Describe the morphology of the red blood cells.
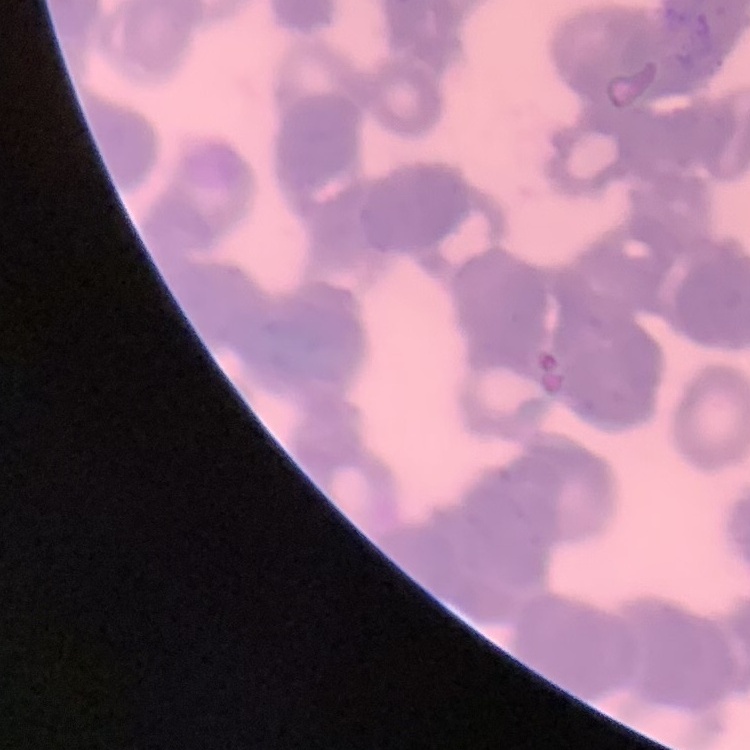

They show rouleaux formation.

{
  "preparation": "thin peripheral smear",
  "stain": "Field's or Giemsa",
  "image_type": "square crop of a larger photomicrograph"
}